Describe the morphology of the red blood cells.
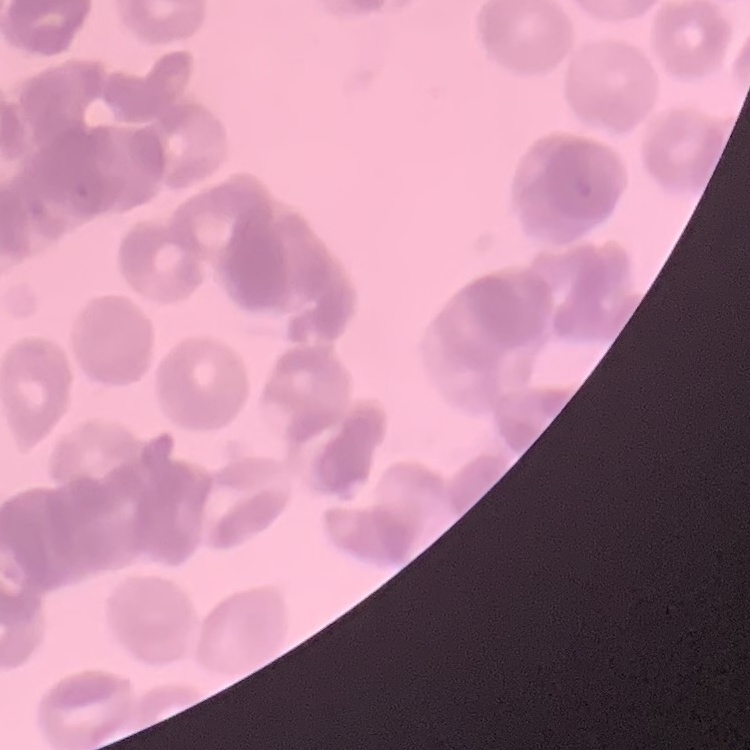

Rouleaux formation.

Stained with either Field's or Giemsa. Thin blood film. One tile cut from a larger photomicrograph.